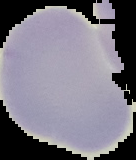
Summary:
  - Malaria status: uninfected
  - Image size: 136×160 pixels
  - Image type: segmented cell region on a black background
  - Preparation: thin blood smear